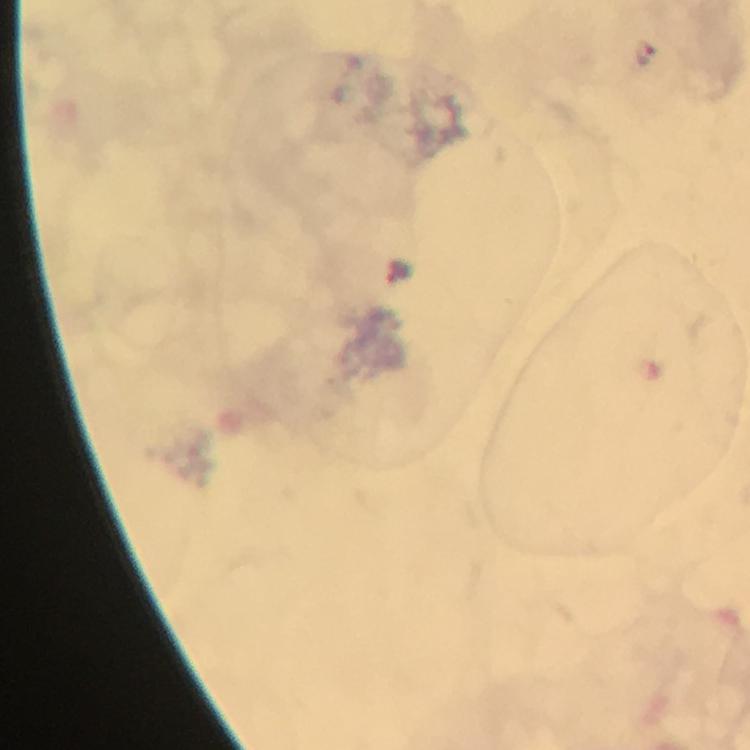

Approximate object centers, in pixels from the top-left corner.
Summary:
  - Plasmodium parasite locations: (x=647, y=53)
  - Preparation: thick blood smear
  - Magnification: 100x
  - Capture: smartphone camera through the microscope
  - Stain: Giemsa
  - Image size: 750×750 pixels
  - Immersion oil: used
  - Context: from a malaria diagnostic workup
  - Cropped from: a single field of view